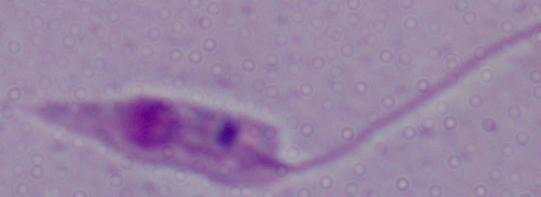
A Leishmania parasite is seen. Captured at 1000x magnification. Photomicrograph.